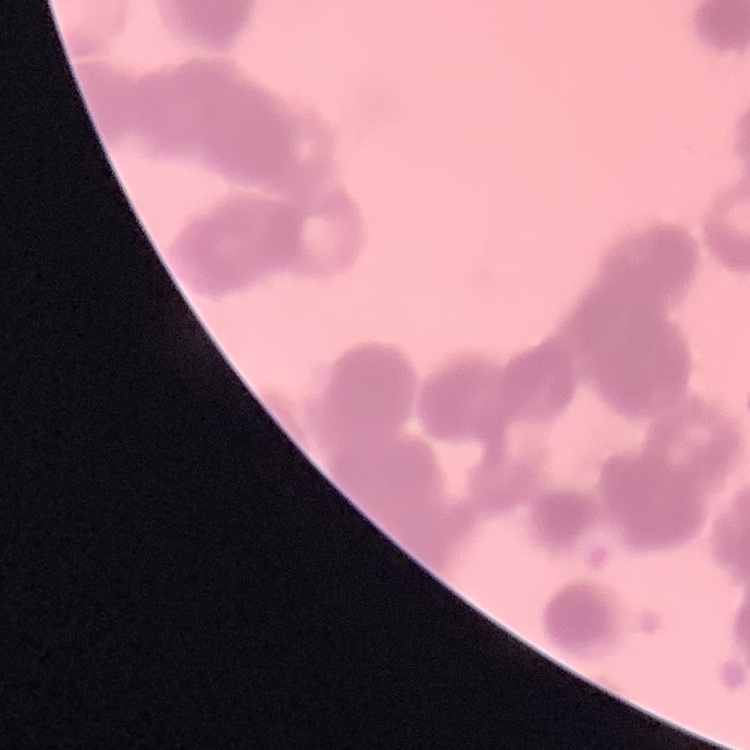

Summary:
  - Red blood cell morphology: rouleaux formation
  - Stain: Field's or Giemsa
  - Preparation: thin peripheral smear
  - Image type: one tile cut from a larger photomicrograph